Identify the blood parasite species.
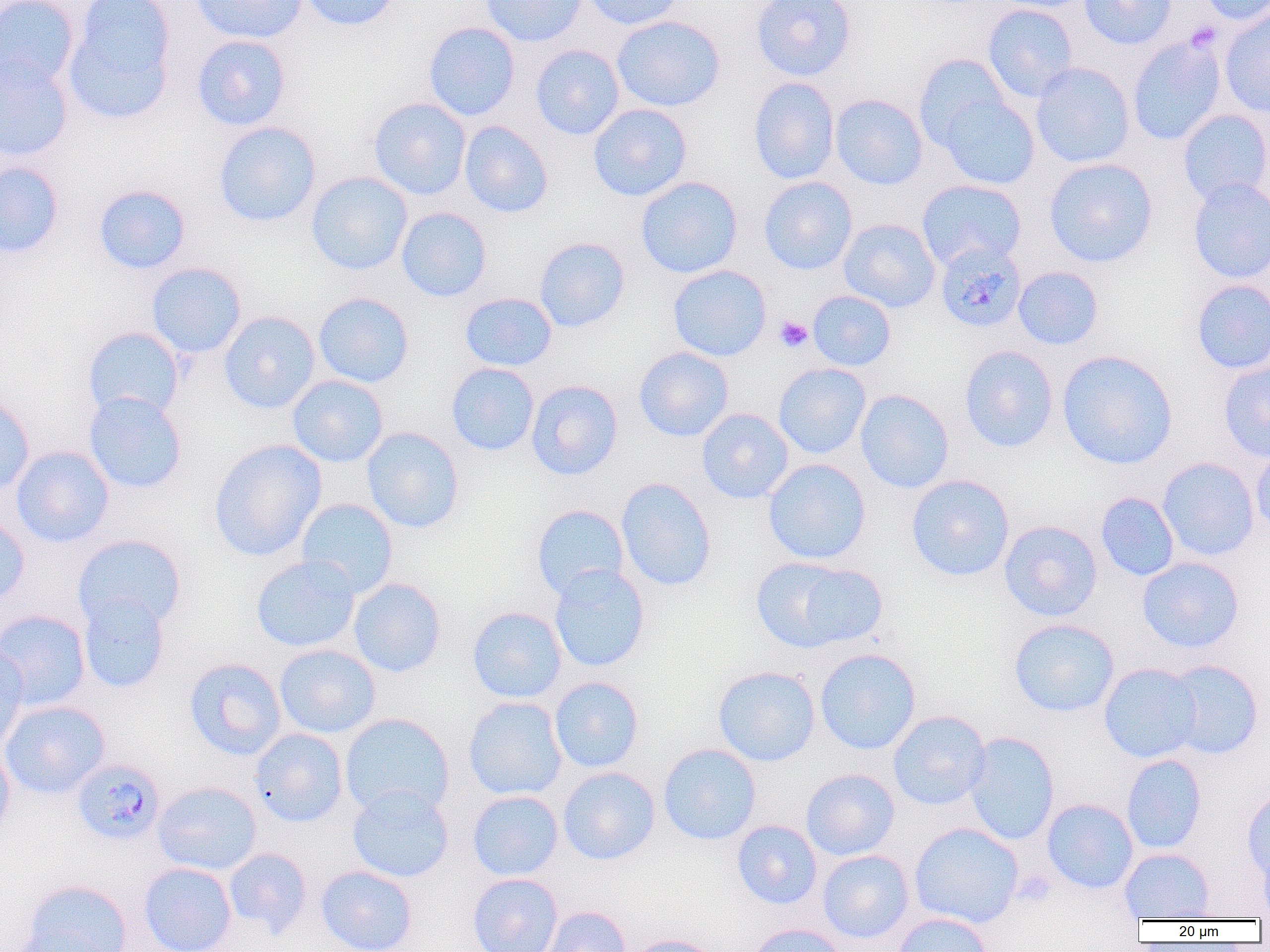
Plasmodium malariae.

magnification = 1000x
preparation = thin blood film
field of view = single
platelet locations = approximate bounding boxes as (x1,y1)-(x2,y2) corner pairs in pixels: (775,315)-(813,352)
Plasmodium malariae-infected red blood cell locations = approximate bounding boxes as (x1,y1)-(x2,y2) corner pairs in pixels: (935,241)-(1027,333), (71,758)-(166,846)
uninfected red blood cell locations = approximate bounding boxes as (x1,y1)-(x2,y2) corner pairs in pixels: (0,0)-(81,92), (189,0)-(308,44), (297,0)-(404,32), (480,0)-(587,46), (581,0)-(687,30), (751,0)-(857,81), (990,0)-(1097,12), (1078,0)-(1176,50), (1195,0)-(1270,25), (62,1)-(177,124), (982,4)-(1079,102), (1218,9)-(1270,118), (612,15)-(725,112), (423,21)-(520,121), (191,35)-(291,131), (1127,35)-(1227,146), (530,44)-(624,140), (913,53)-(1012,150), (0,55)-(73,162), (1030,62)-(1135,169), (748,77)-(839,184), (937,93)-(1040,190), (830,94)-(928,190), (368,97)-(471,200), (588,104)-(692,201), (1177,109)-(1270,207), (213,121)-(321,228), (460,121)-(553,218), (1044,157)-(1158,268), (0,161)-(65,258), (306,171)-(413,275), (636,176)-(743,279), (758,176)-(858,275), (1187,178)-(1270,285), (916,179)-(1026,271), (92,184)-(191,275), (396,207)-(492,302), (838,218)-(940,313), (534,237)-(630,332), (146,262)-(246,358), (668,264)-(771,361), (1013,266)-(1104,350), (1190,279)-(1270,374), (807,290)-(896,371), (313,292)-(414,388), (459,292)-(557,371), (219,311)-(320,414), (83,326)-(184,421), (959,345)-(1059,453), (634,346)-(734,441), (1057,349)-(1178,470), (446,362)-(539,456), (1218,362)-(1270,462), (773,363)-(871,459), (288,375)-(388,467), (526,380)-(623,480), (855,389)-(954,493), (84,392)-(187,494), (0,393)-(35,496), (696,408)-(794,504), (362,427)-(464,533), (208,439)-(327,562), (11,445)-(114,548), (1249,446)-(1270,541), (1157,457)-(1260,561), (763,458)-(871,564), (906,474)-(1015,582), (616,477)-(716,592), (1096,492)-(1180,581), (295,498)-(398,598), (532,505)-(630,599), (0,512)-(30,607), (999,520)-(1102,621), (73,533)-(186,632), (250,555)-(360,653), (751,556)-(883,652), (1137,556)-(1244,653), (548,564)-(650,673), (348,577)-(447,677), (78,593)-(170,693), (467,606)-(567,703), (0,610)-(91,711), (1008,618)-(1120,717), (0,641)-(28,753), (274,644)-(380,739), (814,648)-(921,755), (183,658)-(287,760), (1164,659)-(1264,759), (1099,663)-(1201,763), (712,665)-(820,766), (549,676)-(644,772), (463,696)-(567,800), (0,699)-(110,800), (888,710)-(991,810), (339,713)-(454,819), (249,728)-(348,827), (963,731)-(1060,845), (658,743)-(761,845), (0,744)-(15,843), (1122,754)-(1206,854), (559,757)-(760,849), (557,766)-(660,865), (801,769)-(899,860), (152,781)-(262,875), (347,784)-(454,882), (1241,788)-(1270,882), (467,790)-(563,880), (1042,798)-(1139,893), (732,820)-(822,909), (909,822)-(1024,928), (224,848)-(312,938), (1119,848)-(1215,921), (817,850)-(914,943), (138,862)-(236,952), (316,865)-(418,952), (467,873)-(563,952), (21,879)-(132,952), (540,905)-(631,952), (892,912)-(992,952), (745,923)-(848,952), (8,929)-(114,952), (623,934)-(725,952)
modality = optical microscopy
image size = 1270×952 pixels